Name the blood parasite species.
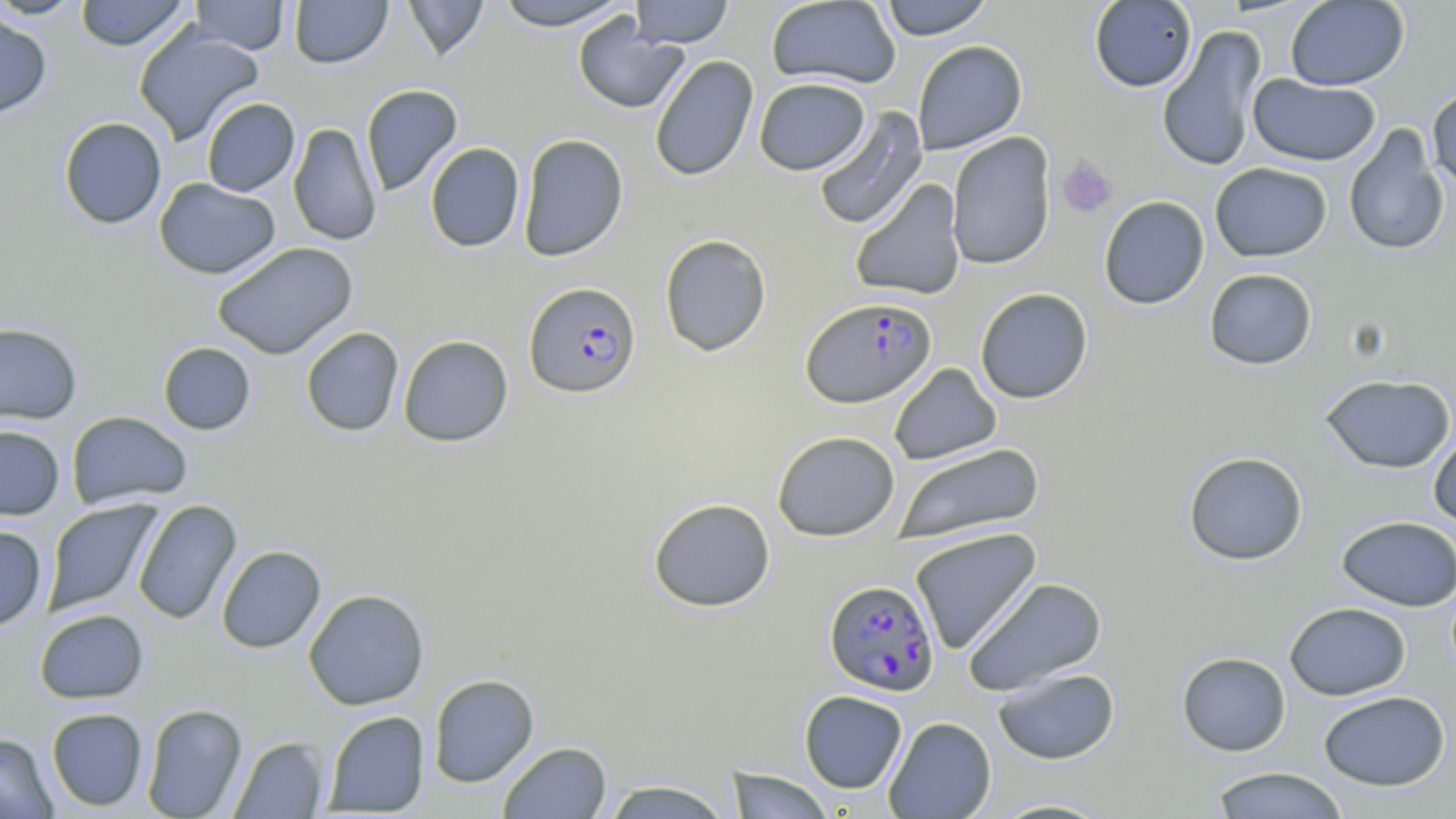
Plasmodium falciparum.

magnification = 1000x
Plasmodium falciparum-infected red blood cell locations = approximate bounding boxes as [x1, y1, x2, y2] in pixels: [523, 281, 641, 398], [801, 296, 937, 408], [824, 579, 940, 696]
modality = optical microscopy
uninfected red blood cell locations = approximate bounding boxes as [x1, y1, x2, y2] in pixels: [0, 0, 88, 20], [74, 0, 191, 51], [189, 0, 290, 55], [289, 0, 393, 68], [401, 0, 491, 61], [765, 0, 902, 89], [877, 0, 994, 40], [1089, 0, 1197, 92], [493, 1, 631, 31], [629, 1, 734, 48], [1285, 1, 1410, 90], [0, 8, 52, 120], [572, 15, 689, 114], [133, 24, 265, 146], [1157, 25, 1267, 173], [912, 40, 1028, 154], [649, 55, 759, 182], [1247, 74, 1381, 166], [754, 77, 870, 175], [360, 84, 463, 196], [1427, 85, 1456, 194], [201, 97, 300, 196], [812, 107, 928, 230], [58, 116, 167, 229], [289, 122, 383, 247], [1343, 124, 1450, 256], [947, 132, 1057, 270], [517, 133, 629, 262], [425, 142, 525, 252], [1210, 162, 1332, 262], [154, 178, 281, 279], [849, 178, 967, 301], [1098, 196, 1210, 310], [659, 234, 772, 356], [212, 242, 357, 360], [1204, 268, 1317, 370], [975, 287, 1093, 404], [0, 323, 82, 424], [300, 327, 404, 436], [398, 335, 514, 447], [157, 341, 256, 435], [889, 363, 1002, 465], [1319, 372, 1456, 474], [66, 411, 192, 510], [0, 425, 65, 519], [1428, 429, 1456, 530], [773, 430, 900, 541], [891, 442, 1045, 546], [1183, 451, 1309, 565], [648, 497, 776, 612], [42, 499, 162, 616], [132, 499, 242, 625], [1336, 515, 1455, 611], [0, 526, 47, 632], [909, 527, 1042, 655], [216, 545, 326, 653], [962, 576, 1107, 696], [303, 589, 429, 710], [1284, 601, 1411, 700], [34, 609, 148, 703], [1176, 651, 1291, 757], [993, 666, 1120, 765], [428, 673, 539, 787], [799, 690, 908, 793], [1318, 690, 1450, 791], [141, 703, 248, 819], [46, 708, 148, 811], [323, 710, 430, 816], [883, 716, 996, 818], [0, 733, 58, 819], [229, 736, 329, 818], [497, 741, 612, 819], [1208, 766, 1350, 818], [725, 768, 836, 818], [600, 779, 734, 819], [985, 797, 1118, 818]
field of view = single
preparation = thin blood film
stain = May-Grünwald-Giemsa
image size = 1456×819 pixels
platelet locations = approximate bounding boxes as [x1, y1, x2, y2] in pixels: [1056, 158, 1117, 218]